Locate and identify every blood parasite.
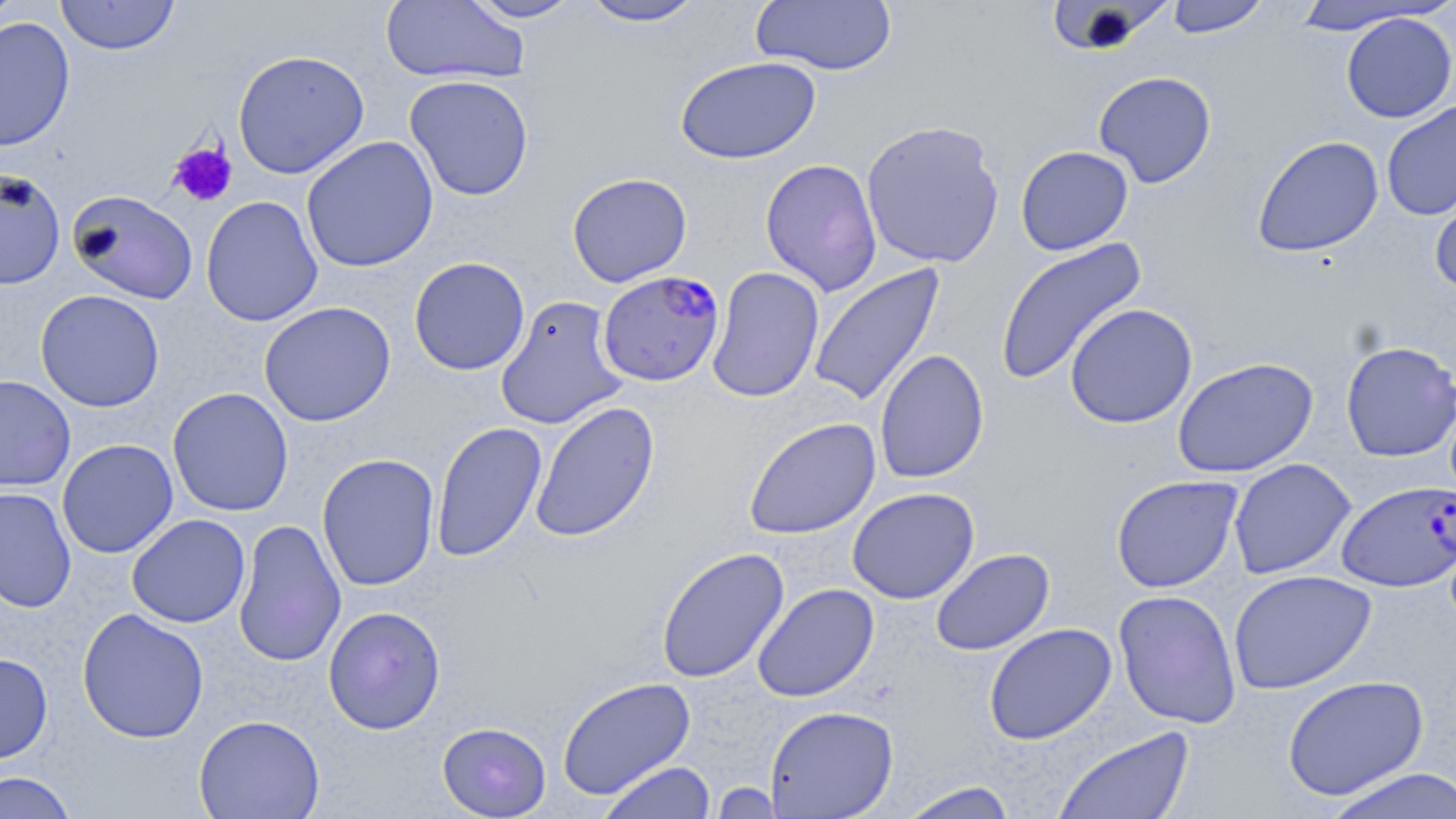
Approximate bounding boxes as named x1/y1/x2/y2 corners in pixels.
Plasmodium falciparum-infected red blood cells: (x1=596, y1=269, x2=725, y2=387), (x1=1336, y1=480, x2=1455, y2=592).
No Plasmodium ovale, Plasmodium malariae, Plasmodium vivax, Babesia divergens, or Trypanosoma brucei observed.

slide-level diagnosis = Plasmodium falciparum
uninfected red blood cell locations = approximate bounding boxes as named x1/y1/x2/y2 corners in pixels: (x1=0, y1=0, x2=27, y2=30), (x1=55, y1=0, x2=180, y2=56), (x1=380, y1=0, x2=529, y2=84), (x1=464, y1=0, x2=586, y2=23), (x1=577, y1=0, x2=709, y2=27), (x1=1164, y1=0, x2=1272, y2=38), (x1=750, y1=1, x2=898, y2=76), (x1=1045, y1=1, x2=1176, y2=56), (x1=1289, y1=1, x2=1439, y2=35), (x1=1340, y1=12, x2=1456, y2=123), (x1=0, y1=16, x2=76, y2=153), (x1=232, y1=49, x2=370, y2=179), (x1=675, y1=56, x2=822, y2=165), (x1=1093, y1=71, x2=1217, y2=188), (x1=404, y1=74, x2=534, y2=201), (x1=1381, y1=99, x2=1456, y2=221), (x1=860, y1=119, x2=1005, y2=269), (x1=301, y1=135, x2=439, y2=273), (x1=1251, y1=135, x2=1384, y2=258), (x1=1015, y1=145, x2=1134, y2=256), (x1=760, y1=158, x2=883, y2=296), (x1=0, y1=169, x2=66, y2=290), (x1=567, y1=172, x2=692, y2=287), (x1=1429, y1=178, x2=1456, y2=296), (x1=68, y1=190, x2=198, y2=304), (x1=200, y1=196, x2=323, y2=327), (x1=994, y1=237, x2=1148, y2=387), (x1=409, y1=256, x2=530, y2=376), (x1=807, y1=262, x2=947, y2=408), (x1=707, y1=266, x2=825, y2=403), (x1=35, y1=289, x2=165, y2=412), (x1=494, y1=295, x2=629, y2=430), (x1=258, y1=302, x2=396, y2=427), (x1=1064, y1=303, x2=1198, y2=429), (x1=1340, y1=340, x2=1456, y2=462), (x1=874, y1=349, x2=990, y2=484), (x1=1172, y1=356, x2=1318, y2=478), (x1=0, y1=375, x2=76, y2=491), (x1=168, y1=387, x2=294, y2=516), (x1=529, y1=400, x2=660, y2=543), (x1=743, y1=417, x2=881, y2=540), (x1=431, y1=421, x2=547, y2=562), (x1=57, y1=439, x2=178, y2=559), (x1=316, y1=453, x2=440, y2=592), (x1=1228, y1=457, x2=1356, y2=580), (x1=1110, y1=474, x2=1243, y2=593), (x1=0, y1=487, x2=77, y2=613), (x1=847, y1=487, x2=979, y2=604), (x1=126, y1=514, x2=250, y2=628), (x1=233, y1=519, x2=346, y2=668), (x1=654, y1=547, x2=790, y2=683), (x1=930, y1=548, x2=1055, y2=655), (x1=1228, y1=569, x2=1377, y2=695), (x1=751, y1=583, x2=879, y2=702), (x1=1113, y1=589, x2=1242, y2=729), (x1=323, y1=606, x2=446, y2=735), (x1=77, y1=608, x2=209, y2=744), (x1=983, y1=623, x2=1117, y2=745), (x1=0, y1=653, x2=53, y2=763), (x1=1282, y1=675, x2=1429, y2=801), (x1=556, y1=676, x2=697, y2=800), (x1=765, y1=705, x2=899, y2=818), (x1=194, y1=714, x2=325, y2=819), (x1=437, y1=721, x2=552, y2=818), (x1=1051, y1=726, x2=1196, y2=819), (x1=598, y1=761, x2=716, y2=819), (x1=1320, y1=768, x2=1456, y2=819), (x1=0, y1=771, x2=78, y2=818), (x1=895, y1=781, x2=1020, y2=819), (x1=709, y1=782, x2=787, y2=818)
image size = 1456×819 pixels
magnification = 1000x
preparation = thin blood film
field of view = single
platelet locations = approximate bounding boxes as named x1/y1/x2/y2 corners in pixels: (x1=168, y1=141, x2=238, y2=207)
stain = May-Grünwald-Giemsa
modality = optical microscopy